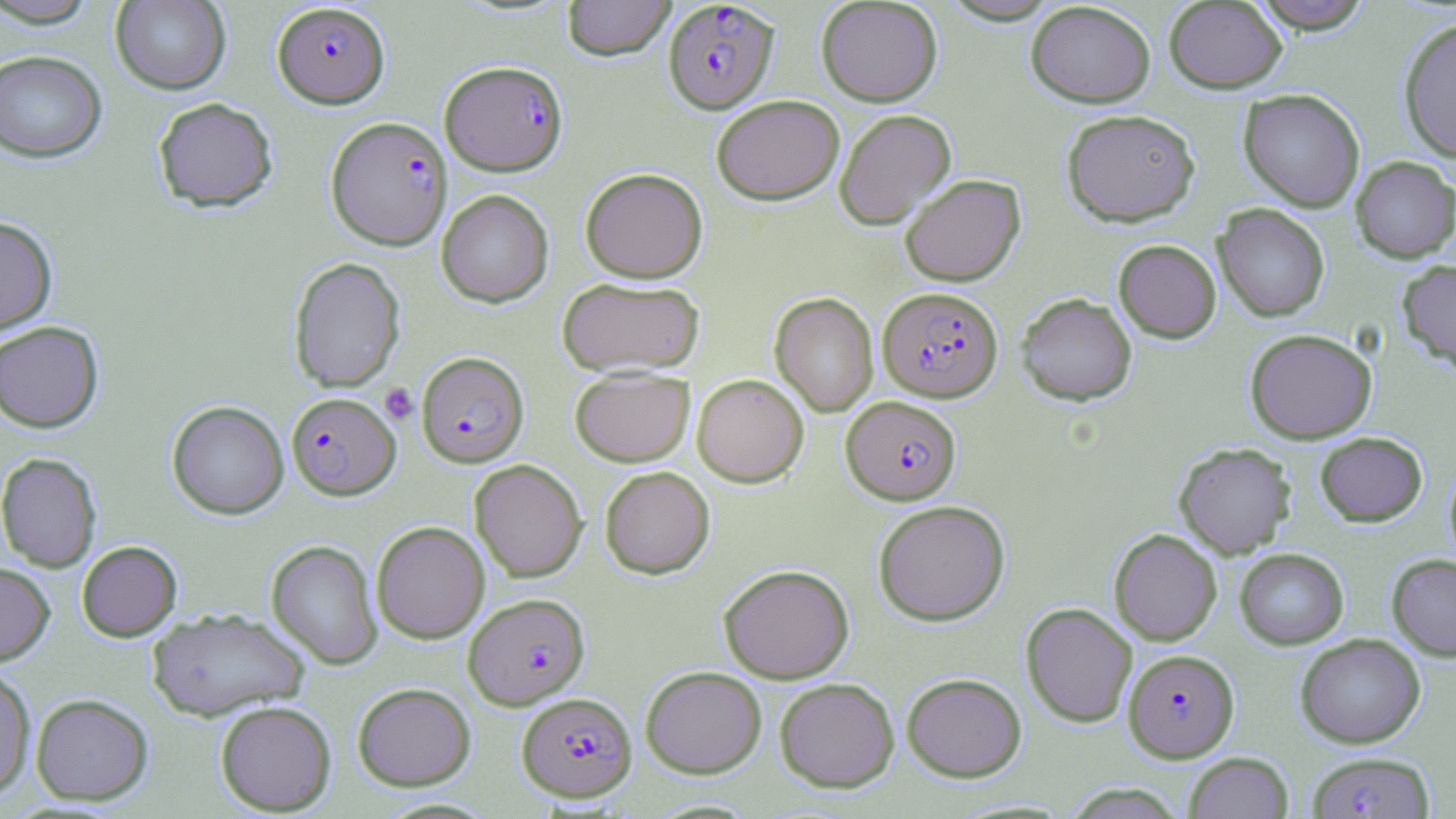

slide-level diagnosis = Plasmodium falciparum
stain = May-Grünwald-Giemsa
magnification = 1000x
image size = 1456×819 pixels
Plasmodium falciparum-infected red blood cell locations = approximate bounding boxes as named x1/y1/x2/y2 corners in pixels: (x1=663, y1=1, x2=779, y2=113), (x1=272, y1=2, x2=390, y2=108), (x1=440, y1=60, x2=567, y2=174), (x1=326, y1=116, x2=453, y2=249), (x1=877, y1=286, x2=1003, y2=402), (x1=416, y1=351, x2=529, y2=467), (x1=286, y1=392, x2=401, y2=500), (x1=842, y1=396, x2=961, y2=504), (x1=464, y1=593, x2=590, y2=709), (x1=1123, y1=649, x2=1239, y2=762), (x1=517, y1=692, x2=637, y2=801), (x1=1307, y1=751, x2=1435, y2=818)
modality = light microscopy
platelet locations = approximate bounding boxes as named x1/y1/x2/y2 corners in pixels: (x1=380, y1=383, x2=419, y2=424)
preparation = thin blood smear
uninfected red blood cell locations = approximate bounding boxes as named x1/y1/x2/y2 corners in pixels: (x1=1, y1=0, x2=104, y2=28), (x1=110, y1=0, x2=231, y2=94), (x1=562, y1=0, x2=676, y2=60), (x1=816, y1=0, x2=943, y2=106), (x1=938, y1=0, x2=1064, y2=25), (x1=1250, y1=0, x2=1374, y2=33), (x1=1164, y1=1, x2=1288, y2=93), (x1=1026, y1=2, x2=1156, y2=107), (x1=1398, y1=17, x2=1456, y2=160), (x1=0, y1=50, x2=108, y2=162), (x1=1238, y1=89, x2=1365, y2=212), (x1=711, y1=94, x2=845, y2=204), (x1=152, y1=97, x2=278, y2=213), (x1=834, y1=108, x2=956, y2=229), (x1=1061, y1=108, x2=1200, y2=226), (x1=1351, y1=156, x2=1456, y2=263), (x1=580, y1=167, x2=708, y2=283), (x1=899, y1=174, x2=1025, y2=287), (x1=436, y1=189, x2=554, y2=307), (x1=1213, y1=203, x2=1330, y2=322), (x1=0, y1=216, x2=58, y2=336), (x1=1113, y1=239, x2=1222, y2=343), (x1=288, y1=257, x2=405, y2=393), (x1=1397, y1=259, x2=1456, y2=376), (x1=557, y1=276, x2=706, y2=377), (x1=770, y1=292, x2=879, y2=417), (x1=1016, y1=293, x2=1138, y2=406), (x1=0, y1=320, x2=104, y2=433), (x1=1245, y1=328, x2=1376, y2=443), (x1=569, y1=367, x2=694, y2=466), (x1=692, y1=373, x2=808, y2=487), (x1=167, y1=400, x2=289, y2=519), (x1=1315, y1=432, x2=1427, y2=527), (x1=1174, y1=442, x2=1296, y2=558), (x1=0, y1=452, x2=101, y2=572), (x1=1445, y1=457, x2=1456, y2=575), (x1=470, y1=459, x2=587, y2=582), (x1=599, y1=466, x2=715, y2=579), (x1=872, y1=500, x2=1010, y2=625), (x1=371, y1=521, x2=489, y2=643), (x1=1109, y1=529, x2=1222, y2=646), (x1=266, y1=540, x2=383, y2=669), (x1=77, y1=541, x2=182, y2=641), (x1=1234, y1=548, x2=1349, y2=649), (x1=1387, y1=554, x2=1456, y2=661), (x1=0, y1=563, x2=54, y2=666), (x1=718, y1=563, x2=854, y2=683), (x1=1021, y1=602, x2=1138, y2=727), (x1=147, y1=607, x2=310, y2=722), (x1=1295, y1=633, x2=1425, y2=748), (x1=640, y1=665, x2=767, y2=778), (x1=0, y1=666, x2=36, y2=800), (x1=902, y1=672, x2=1027, y2=782), (x1=774, y1=677, x2=900, y2=793), (x1=352, y1=682, x2=476, y2=790), (x1=31, y1=693, x2=153, y2=805), (x1=214, y1=700, x2=337, y2=816), (x1=1183, y1=752, x2=1294, y2=819), (x1=1062, y1=783, x2=1188, y2=818)
field of view = one of a larger specimen